Report the malaria status of this cell.
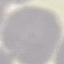
Uninfected.

stain: Giemsa
preparation: thin smear
capture: smartphone through the microscope eyepiece
image_type: cell patch, automatically extracted from a larger field of view and resized to 64 × 64 pixels